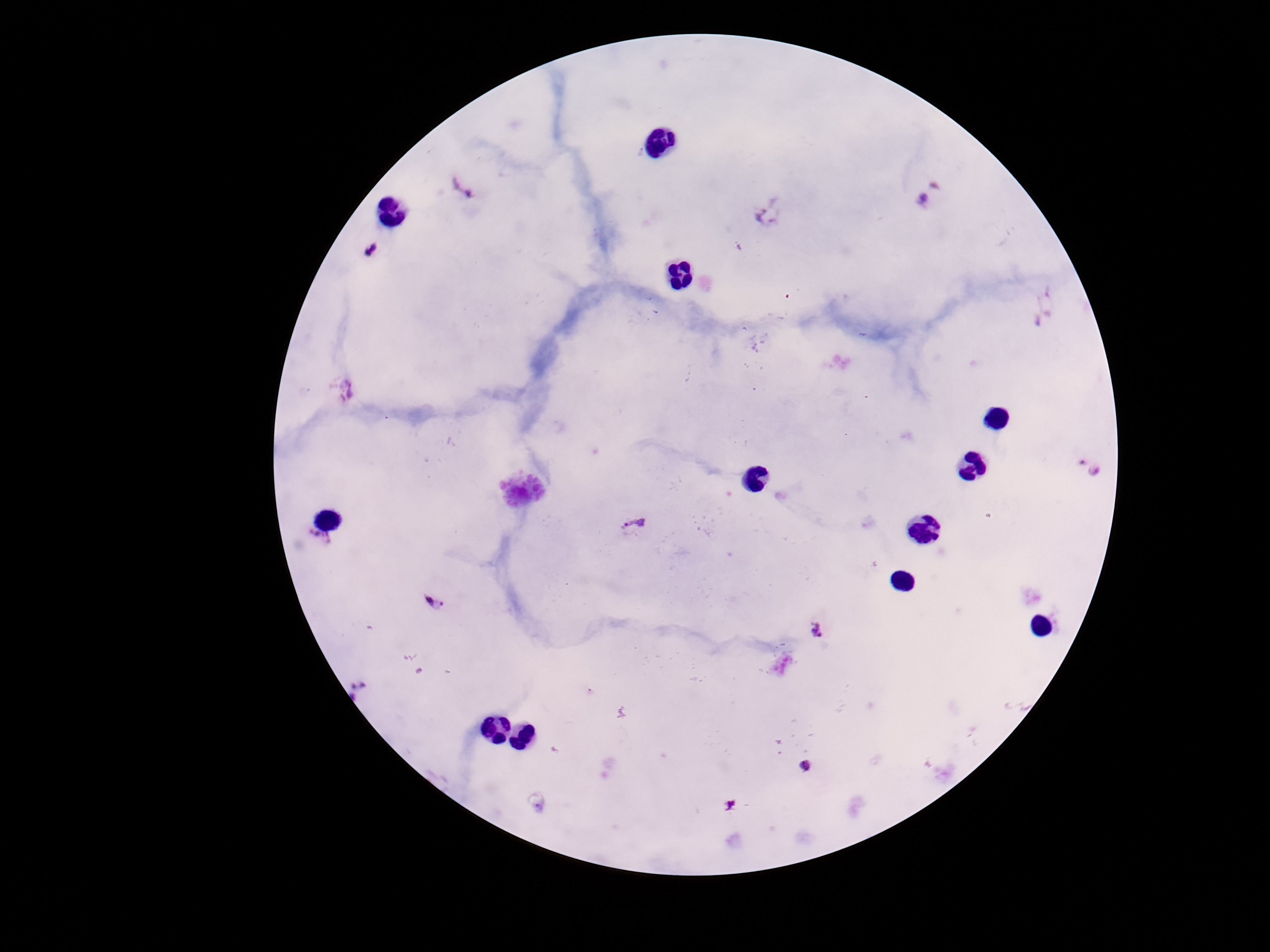

Approximate centers as {x, y} in pixels. Plasmodium parasite locations: {461, 187}, {933, 196}, {772, 214}, {367, 252}, {1045, 309}, {345, 390}, {1087, 465}, {635, 526}, {319, 541}, {433, 604}, {824, 633}, {361, 688}, {805, 768}. One field from this slide. Image is 1270×952 pixels. Smartphone photograph taken through the microscope eyepiece. Giemsa-stained preparation. Thick blood film. 100x magnification. Patient malaria status: positive.